Classify this cell by malaria status.
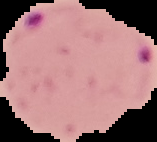

It is parasitized.

image_size: 157×142 pixels
preparation: thin blood smear
image_type: cell region segmented out of the field of view; surrounding area masked to black